Report the malaria status of this cell.
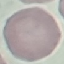

It is uninfected.

stain = Giemsa
capture = smartphone through the microscope eyepiece
image type = automatically extracted cell patch, resized to 64 × 64 pixels
preparation = thin smear